Report the malaria status of this cell.
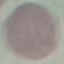

It is uninfected.

Summary:
  - Image type: cell patch, automatically extracted from a larger field of view and resized to 64 × 64 pixels
  - Capture: smartphone camera at the microscope eyepiece
  - Stain: Giemsa
  - Preparation: thin blood smear